State which parasite is depicted.
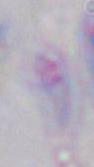

Toxoplasma gondii.

modality = micrograph
magnification = 1000x